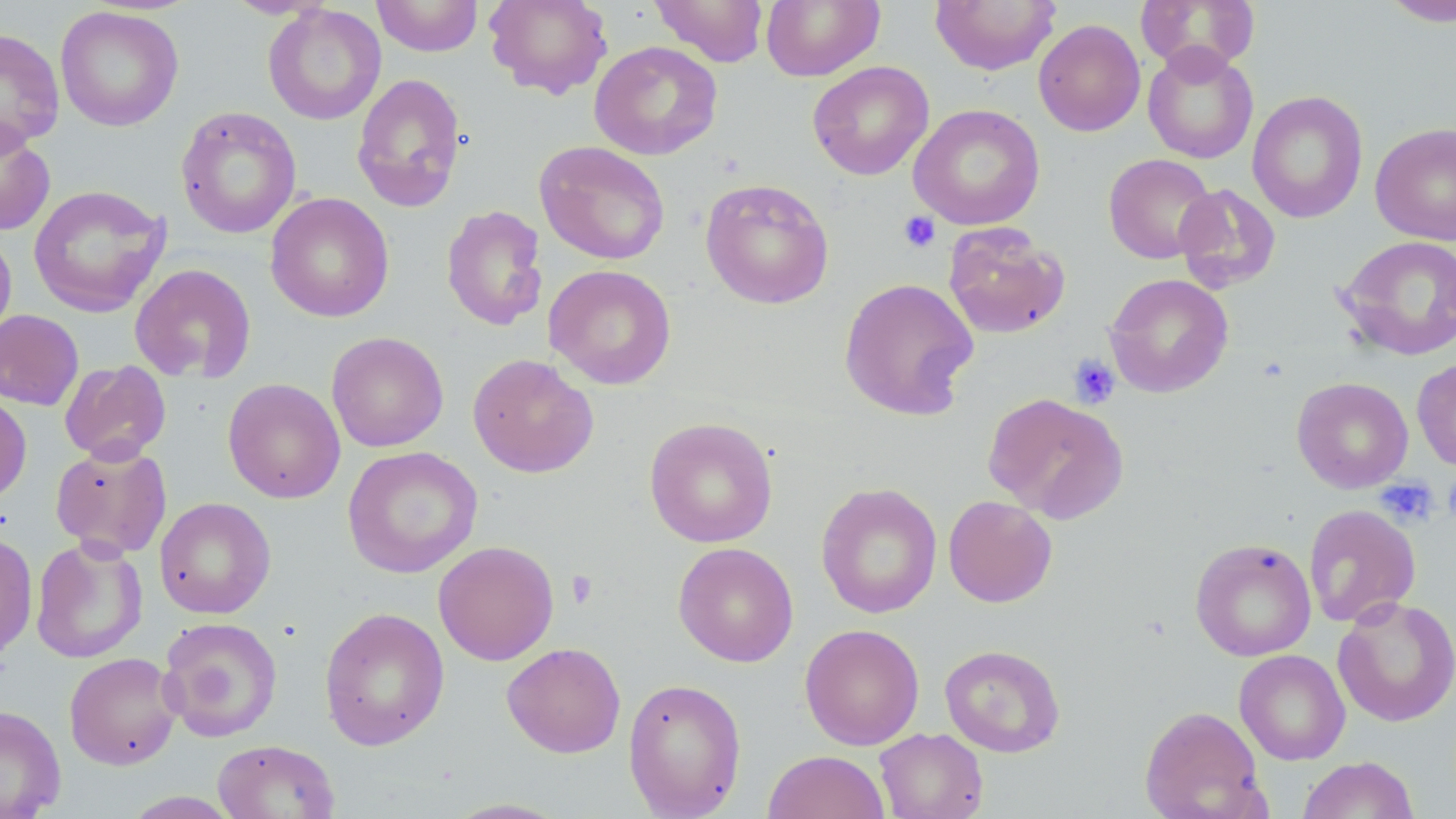

Summary:
  - Coordinate format: approximate bounding boxes as (x1, y1, x2, y2) in pixels
  - Uninfected red blood cell locations: (223, 0, 335, 19), (371, 0, 483, 57), (484, 0, 613, 100), (649, 0, 769, 67), (761, 0, 885, 81), (1134, 0, 1261, 76), (1378, 0, 1456, 27), (930, 1, 1060, 75), (262, 3, 386, 126), (55, 6, 184, 131), (1033, 19, 1146, 136), (0, 28, 65, 153), (590, 41, 722, 160), (1142, 45, 1259, 163), (808, 61, 934, 180), (351, 72, 467, 212), (1247, 91, 1368, 223), (908, 103, 1046, 230), (176, 106, 301, 239), (0, 120, 56, 236), (1370, 122, 1456, 245), (535, 141, 670, 265), (1103, 153, 1217, 264), (700, 178, 834, 310), (1173, 183, 1281, 293), (28, 184, 170, 317), (265, 192, 394, 323), (441, 205, 547, 331), (943, 223, 1070, 338), (0, 229, 17, 345), (1338, 234, 1456, 361), (130, 263, 257, 384), (543, 265, 677, 389), (1104, 273, 1234, 397), (838, 277, 979, 421), (0, 309, 84, 410), (326, 331, 449, 452), (467, 353, 599, 478), (1411, 356, 1456, 472), (59, 360, 172, 464), (1291, 377, 1413, 493), (223, 378, 345, 504), (0, 392, 32, 506), (983, 392, 1129, 523), (644, 417, 778, 548), (50, 442, 172, 559), (343, 446, 483, 578), (816, 482, 942, 618), (943, 495, 1057, 607), (154, 497, 275, 618), (1303, 504, 1421, 627), (0, 531, 38, 661), (30, 536, 148, 664), (1189, 538, 1317, 661), (433, 540, 559, 665), (673, 542, 799, 667), (1332, 595, 1456, 728), (319, 606, 450, 751), (158, 616, 283, 742), (800, 623, 925, 750), (502, 642, 626, 758), (939, 643, 1066, 757), (1234, 649, 1350, 765), (64, 652, 182, 770), (623, 677, 747, 819), (0, 705, 66, 819), (1139, 705, 1269, 819), (875, 727, 989, 819), (212, 739, 340, 818), (762, 750, 890, 818), (1297, 756, 1420, 819), (121, 791, 242, 818), (439, 798, 573, 818)
  - Platelet locations: (898, 211, 941, 253), (1068, 354, 1120, 409), (1443, 472, 1456, 526), (1375, 478, 1439, 527), (566, 570, 599, 609)
  - Slide-level diagnosis: no evidence of blood parasites
  - Magnification: 1000x
  - Stain: May-Grünwald-Giemsa
  - Image size: 1456×819 pixels
  - Preparation: thin blood film
  - Field of view: one of a larger specimen
  - Modality: light microscopy